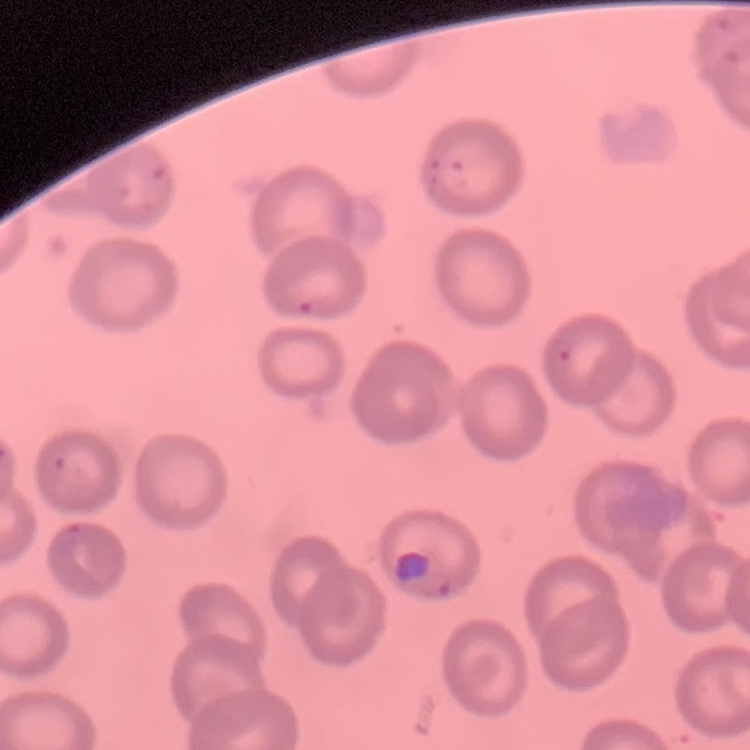
red blood cell morphology = no rouleaux formation
image type = square crop of a larger photomicrograph
stain = Field's or Giemsa
preparation = thin blood smear